Report the malaria status of this cell.
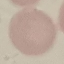

Uninfected.

image_type: cell patch, automatically extracted from a larger field of view and resized to 64 × 64 pixels
capture: smartphone camera at the microscope eyepiece
preparation: thin blood smear
stain: Giemsa